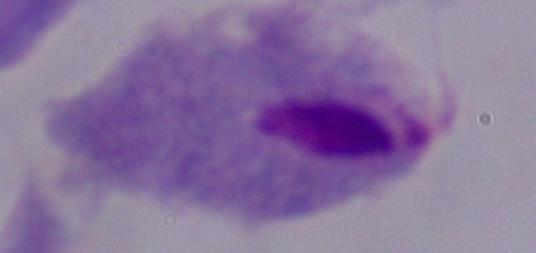
identification = trichomonad
magnification = 1000x
modality = micrograph